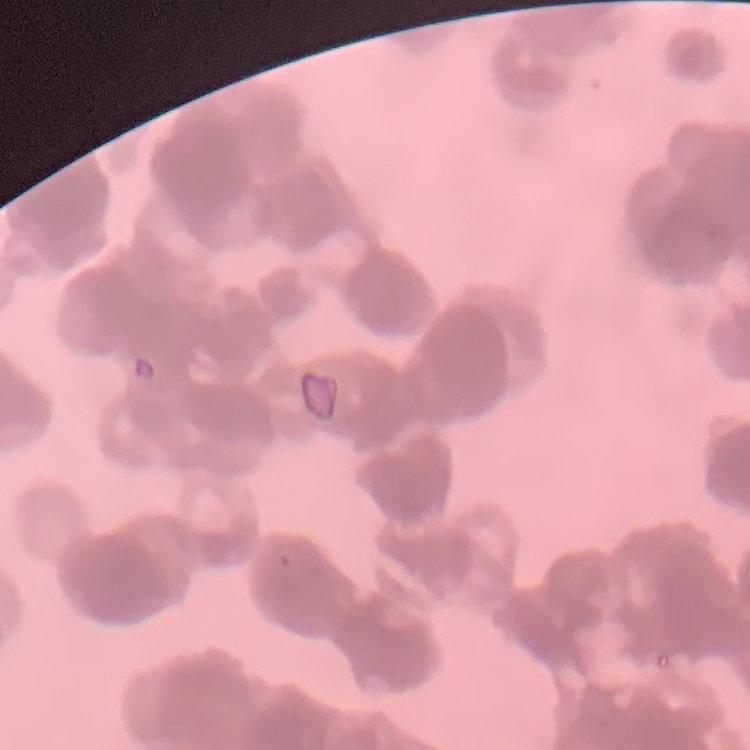

{
  "erythrocyte_morphology": "rouleaux formation",
  "preparation": "thin peripheral smear",
  "image_type": "one tile cut from a larger photomicrograph",
  "stain": "Field's or Giemsa"
}